Give the position of every Plasmodium parasite.
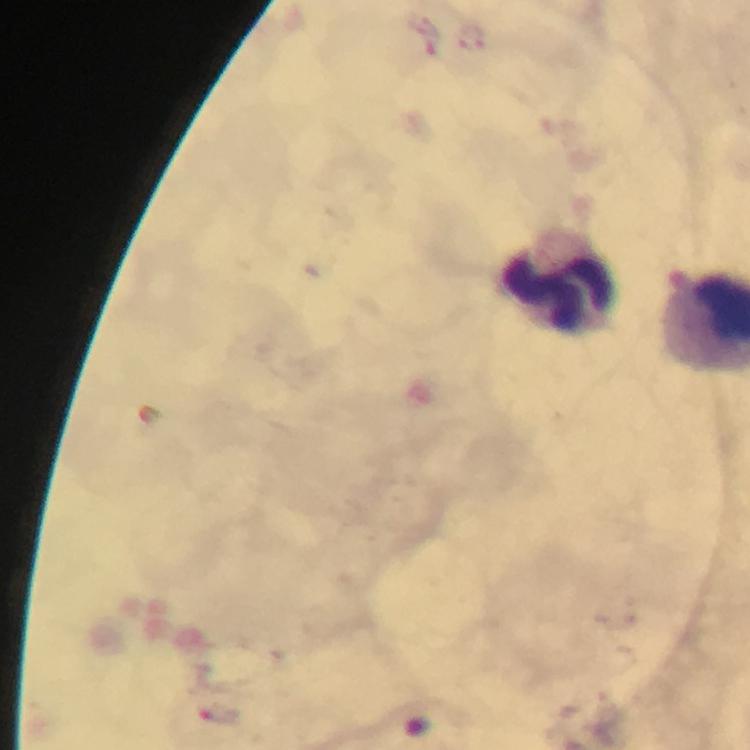

Approximate centers as [x, y] in pixels.
Plasmodium parasites: [473, 37].

Leukocyte locations: [556, 282]. From a malaria diagnostic workup. Image is 750×750 pixels. Photographed through the microscope with a smartphone camera. Immersion oil was used. A crop from one field of view. Giemsa stain. At 100x magnification. Thick blood smear.